Give the extent of all uninfected red blood cells.
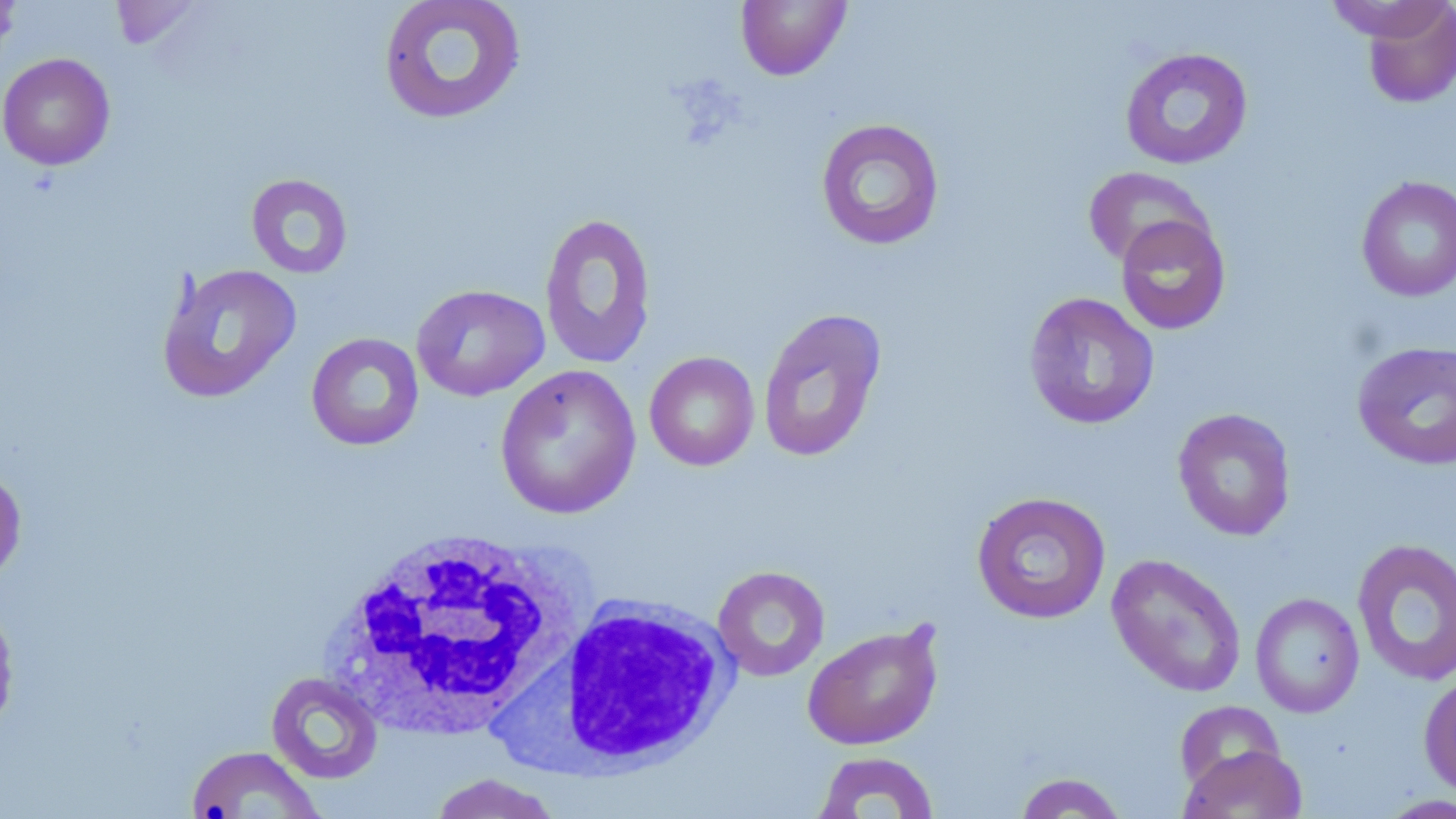

Approximate bounding boxes as (x1, y1, x2, y2) in pixels.
Uninfected red blood cells: (0, 0, 21, 60), (378, 0, 528, 126), (1329, 0, 1452, 51), (111, 1, 205, 51), (735, 1, 852, 81), (1357, 1, 1455, 109), (1119, 47, 1254, 170), (0, 52, 116, 171), (815, 118, 946, 251), (1082, 167, 1213, 269), (245, 173, 354, 279), (1355, 175, 1456, 302), (539, 212, 658, 370), (1115, 215, 1231, 335), (155, 263, 302, 404), (411, 284, 549, 402), (1023, 292, 1160, 430), (757, 307, 887, 464), (306, 332, 424, 451), (1351, 341, 1456, 471), (644, 351, 760, 471), (494, 364, 641, 519), (1172, 407, 1296, 542), (0, 464, 27, 585), (971, 491, 1111, 625), (1351, 538, 1456, 686), (1106, 553, 1247, 698), (713, 565, 830, 681), (1250, 592, 1365, 717), (0, 598, 20, 738), (802, 622, 945, 750), (1418, 670, 1456, 801), (265, 671, 384, 785), (1173, 700, 1286, 791), (1180, 744, 1308, 819), (185, 745, 326, 819), (810, 751, 941, 818), (1013, 771, 1130, 818), (426, 773, 565, 818), (1374, 793, 1456, 818).

White blood cell locations: (324, 527, 584, 742), (492, 594, 741, 772). Slide-level diagnosis: negative for blood parasites. 1000x magnification. Image is 1456×819 pixels. May-Grünwald-Giemsa stain. Light microscopy. Thin blood film. One field of a larger specimen.